Identify the blood parasite species.
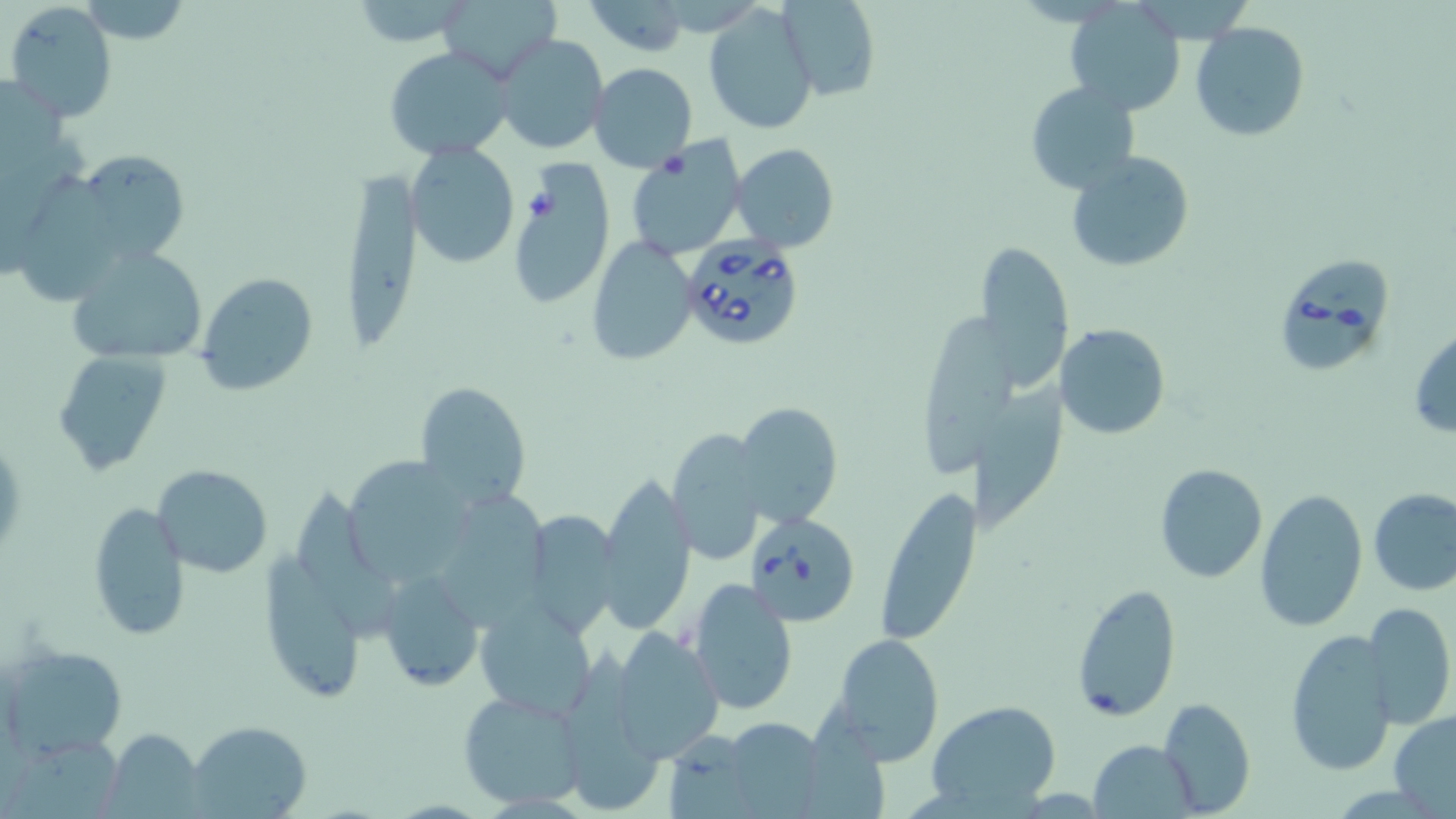
Babesia divergens.

Summary:
  - Coordinate format: approximate bounding boxes as (x1, y1, x2, y2) in pixels
  - Uninfected red blood cell locations: (347, 0, 478, 49), (436, 0, 559, 82), (582, 0, 691, 54), (778, 0, 880, 100), (5, 1, 119, 119), (703, 3, 818, 134), (1066, 3, 1186, 115), (1190, 21, 1311, 142), (496, 33, 607, 155), (385, 46, 515, 161), (588, 62, 698, 173), (1026, 82, 1142, 196), (625, 139, 746, 260), (731, 143, 839, 253), (407, 144, 520, 267), (56, 149, 191, 273), (1066, 151, 1196, 272), (343, 167, 425, 347), (506, 168, 615, 309), (20, 171, 115, 308), (587, 236, 697, 367), (976, 238, 1073, 390), (66, 246, 210, 369), (196, 271, 319, 395), (925, 312, 1017, 477), (1056, 323, 1172, 441), (1409, 326, 1456, 438), (56, 351, 176, 477), (414, 380, 535, 508), (972, 385, 1075, 526), (733, 401, 841, 528), (664, 432, 765, 561), (339, 455, 479, 581), (1154, 464, 1269, 584), (152, 466, 272, 578), (593, 472, 697, 633), (298, 479, 393, 640), (873, 487, 981, 643), (1255, 488, 1367, 634), (1368, 488, 1456, 596), (444, 489, 546, 629), (86, 502, 188, 642), (521, 510, 622, 637), (259, 543, 362, 704), (376, 569, 485, 692), (687, 578, 798, 714), (1069, 580, 1182, 723), (1362, 602, 1455, 729), (475, 604, 596, 720), (611, 629, 724, 761), (1284, 629, 1397, 777), (828, 633, 947, 764), (563, 643, 675, 811), (5, 646, 128, 756), (458, 689, 586, 810), (1157, 696, 1255, 817), (925, 701, 1061, 814), (811, 703, 891, 819), (1390, 709, 1456, 814), (719, 717, 830, 817), (188, 721, 312, 817), (662, 729, 758, 818), (102, 730, 204, 818), (1, 733, 126, 819), (1090, 738, 1196, 817)
  - Babesia divergens-infected red blood cell locations: (677, 234, 807, 351), (1272, 256, 1394, 378), (745, 512, 860, 626)
  - Preparation: thin blood smear
  - Image size: 1456×819 pixels
  - Field of view: single
  - Magnification: 1000x
  - Stain: May-Grünwald-Giemsa
  - Modality: light microscopy